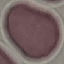
result = no malaria parasites seen
preparation = thin blood film
image type = cell patch, automatically extracted from a larger field of view and resized to 64 × 64 pixels
capture = smartphone camera at the microscope eyepiece
stain = Giemsa